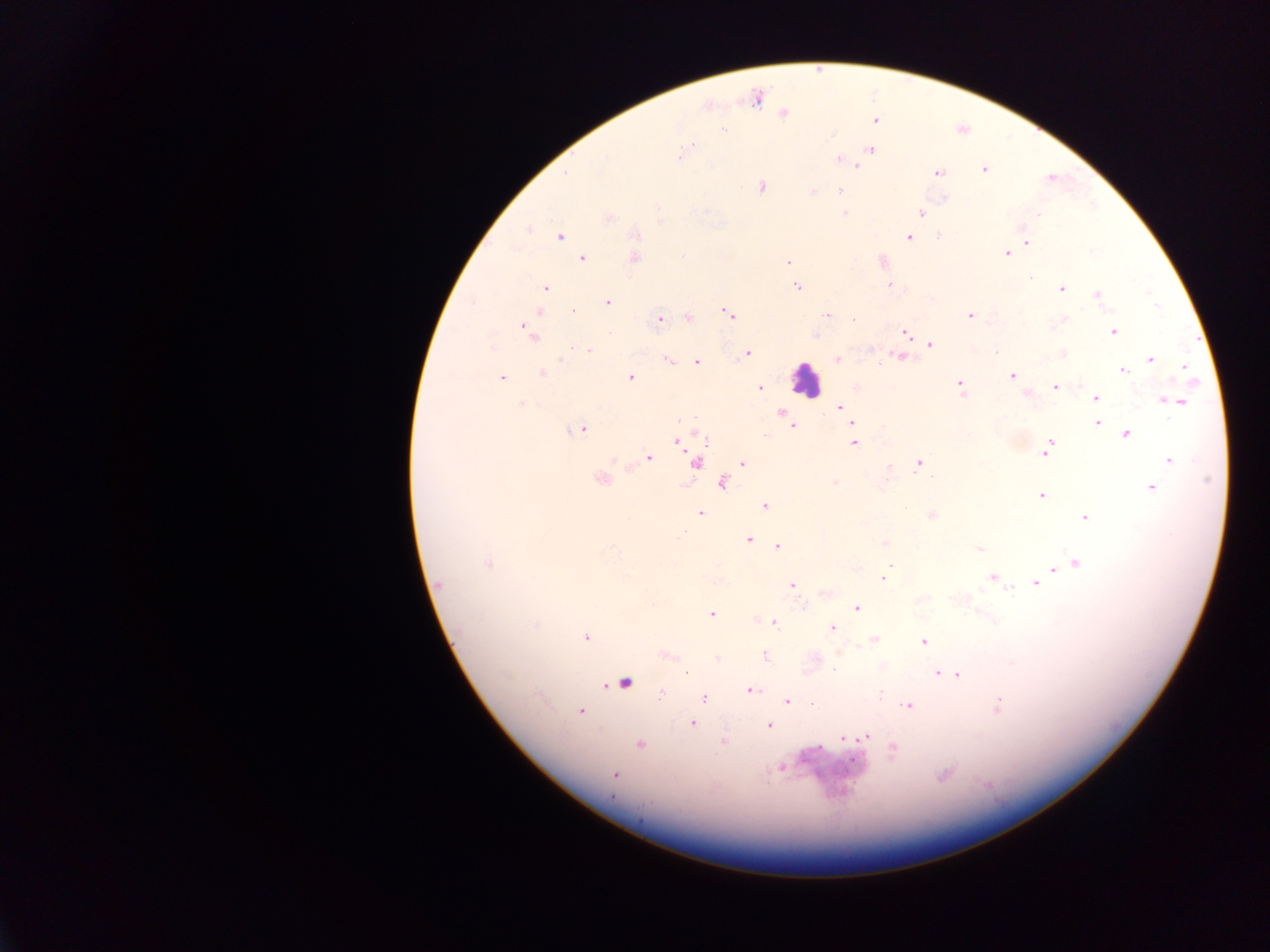
preparation = thick blood film
leukocyte locations = approximate centers as [x, y] in pixels: [806, 379]
image size = 1270×952 pixels
capture = mobile-phone photograph through a microscope
field of view = single
country = Ghana
Plasmodium parasite locations = approximate centers as [x, y] in pixels: [756, 98], [783, 114], [875, 120], [692, 148], [869, 149], [682, 152], [839, 159], [855, 165], [984, 169], [937, 172], [1051, 179], [761, 186], [839, 190], [813, 191], [845, 212], [921, 212], [607, 218], [637, 234], [938, 235], [559, 236], [909, 237], [1026, 241], [1007, 252], [633, 257], [582, 258], [882, 261], [788, 262], [890, 284], [797, 287], [545, 288], [1060, 288], [1097, 295], [607, 303], [728, 312], [827, 313], [971, 314], [687, 317], [659, 319], [854, 320], [527, 329], [1113, 330], [906, 332], [929, 345], [589, 350], [748, 352], [995, 352], [1062, 354], [900, 356], [835, 359], [1149, 359], [668, 360], [697, 360], [1184, 367], [1123, 370], [542, 373], [1011, 376], [629, 377], [500, 378], [959, 384], [1054, 386], [760, 388], [1095, 398], [1167, 400], [1177, 401], [521, 404], [840, 406], [783, 414], [852, 423], [1097, 423], [791, 424], [582, 428], [1126, 433], [764, 434], [677, 439], [852, 442], [1050, 442], [1046, 450], [648, 457], [1170, 460], [695, 462], [742, 463], [918, 463], [600, 479], [722, 482], [835, 482], [1150, 488], [1041, 495], [765, 505], [699, 512], [931, 515], [1085, 517], [748, 539], [883, 543], [778, 545], [979, 548], [487, 563], [1077, 563], [1054, 568], [993, 576], [884, 578], [1034, 582], [791, 585], [825, 591], [856, 607], [710, 613], [774, 623], [830, 628], [586, 637], [873, 638], [923, 640], [765, 655], [666, 656], [718, 658], [834, 669], [686, 673], [938, 673], [949, 673], [957, 674], [623, 683], [748, 690], [703, 697], [787, 701], [908, 705], [996, 708], [579, 711], [691, 723], [768, 726], [865, 737], [844, 739], [723, 741], [639, 745], [893, 750], [781, 768], [615, 774], [944, 776]